Locate every blood parasite and identify its species.
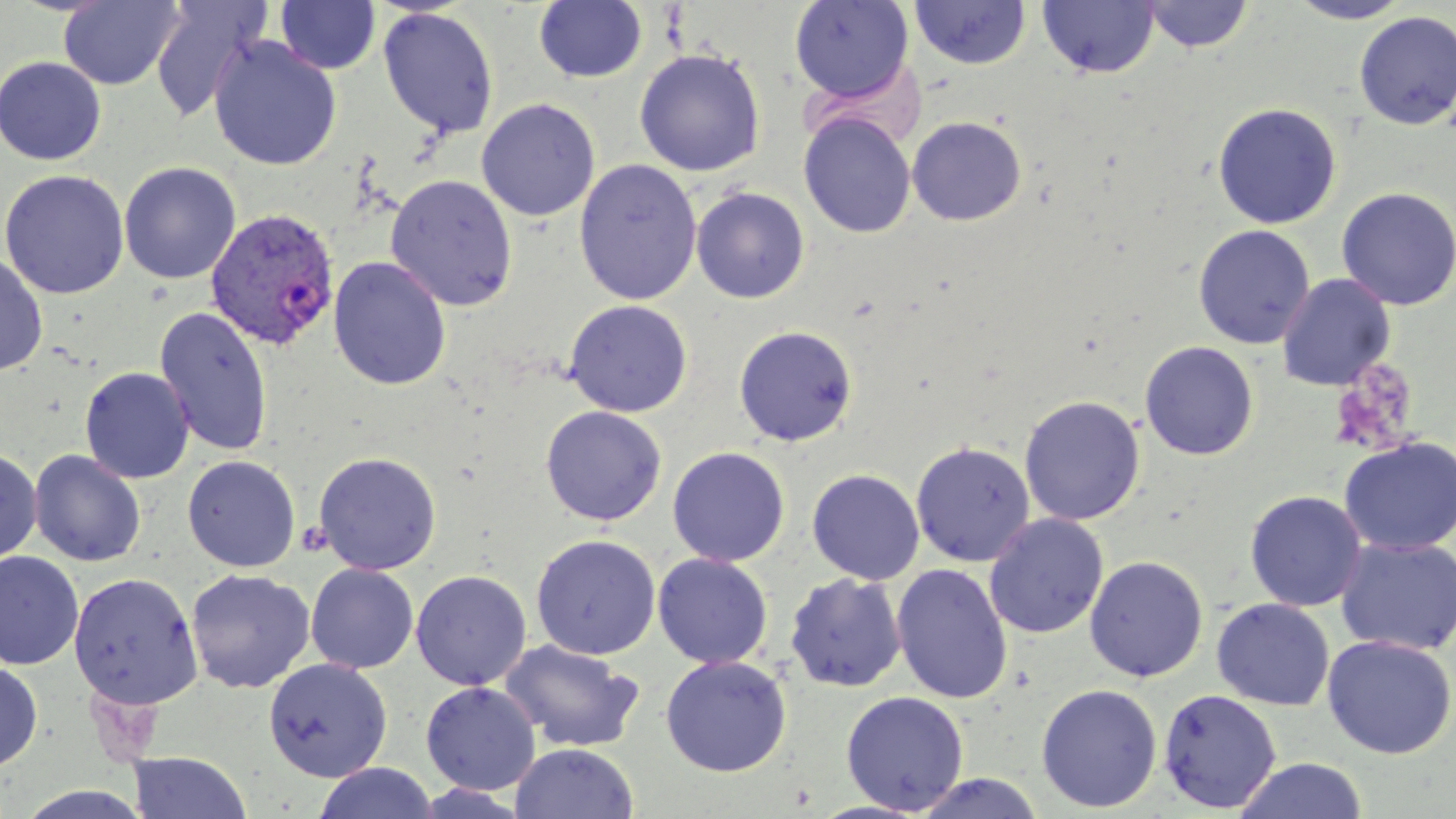
Approximate bounding boxes as (x1,y1)-(x2,y2) corner pairs in pixels.
Plasmodium vivax-infected red blood cells: (207,208)-(340,351).
No Plasmodium falciparum, Plasmodium ovale, Plasmodium malariae, Babesia divergens, or Trypanosoma brucei observed.

Summary:
  - Uninfected red blood cell locations: (789,0)-(914,102), (1038,0)-(1160,79), (1288,0)-(1414,24), (58,1)-(185,90), (148,1)-(269,123), (276,1)-(380,75), (533,1)-(647,83), (910,1)-(1031,70), (1140,1)-(1254,52), (378,6)-(499,139), (1353,11)-(1456,130), (208,36)-(342,171), (634,48)-(765,176), (0,56)-(106,165), (477,98)-(600,221), (1212,102)-(1342,229), (799,111)-(916,239), (906,116)-(1027,226), (574,159)-(702,305), (119,161)-(241,284), (1,169)-(130,299), (385,174)-(518,311), (1336,186)-(1456,311), (692,187)-(810,303), (1192,224)-(1315,349), (0,253)-(48,377), (328,256)-(452,390), (1277,273)-(1396,391), (564,299)-(693,417), (154,305)-(274,457), (733,325)-(858,446), (1139,340)-(1259,461), (80,366)-(194,484), (1019,395)-(1145,525), (540,405)-(666,526), (1338,436)-(1456,555), (910,440)-(1036,567), (667,446)-(790,566), (0,447)-(43,566), (28,450)-(146,567), (313,451)-(442,575), (182,455)-(301,572), (807,469)-(925,585), (1244,490)-(1367,612), (984,513)-(1109,639), (531,534)-(661,660), (1336,535)-(1456,656), (0,552)-(84,670), (652,553)-(773,669), (1084,555)-(1208,682), (891,562)-(1013,705), (306,563)-(419,673), (185,569)-(315,693), (411,569)-(532,690), (69,572)-(203,709), (785,572)-(907,692), (1212,598)-(1334,710), (1322,635)-(1456,758), (499,639)-(645,753), (659,655)-(792,777), (263,658)-(392,781), (0,660)-(43,772), (421,681)-(541,795), (1035,683)-(1163,812), (1158,688)-(1281,813), (840,690)-(969,815), (510,743)-(639,819), (129,751)-(251,818), (1234,758)-(1368,818), (313,763)-(438,819), (911,772)-(1046,818), (17,785)-(152,819)
  - Platelet locations: (1329,362)-(1418,453), (297,521)-(334,556)
  - Slide-level diagnosis: Plasmodium vivax
  - Modality: light microscopy
  - Magnification: 1000x
  - Field of view: single
  - Preparation: thin blood film
  - Image size: 1456×819 pixels
  - Stain: May-Grünwald-Giemsa